Assess this cell for malaria.
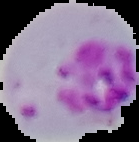

It is parasitized.

Summary:
  - Preparation: thin blood film
  - Image type: segmented cell region with the area outside set to black
  - Image size: 139×142 pixels